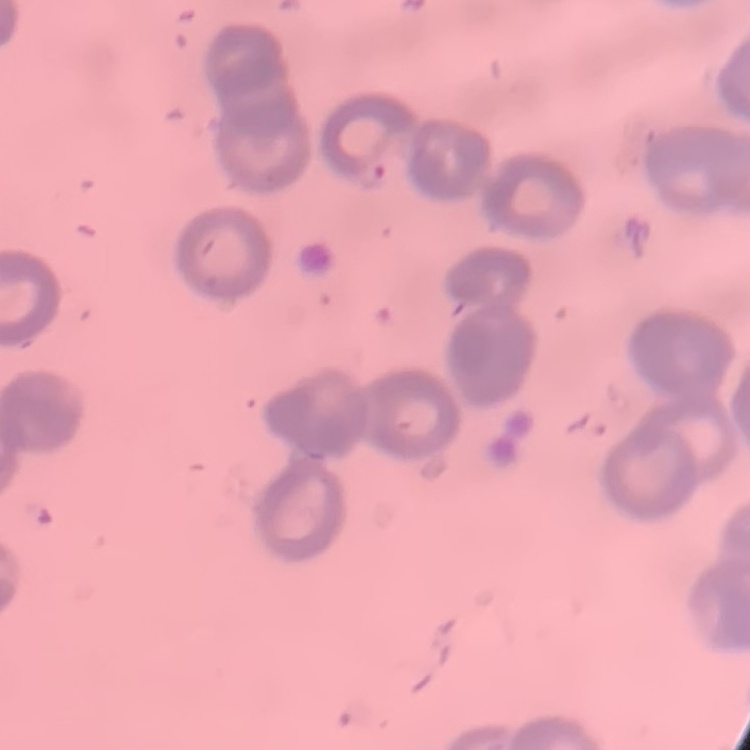

Summary:
  - Erythrocyte morphology: rouleaux formation
  - Image type: square crop of a larger photomicrograph
  - Stain: Field's or Giemsa
  - Preparation: thin blood film